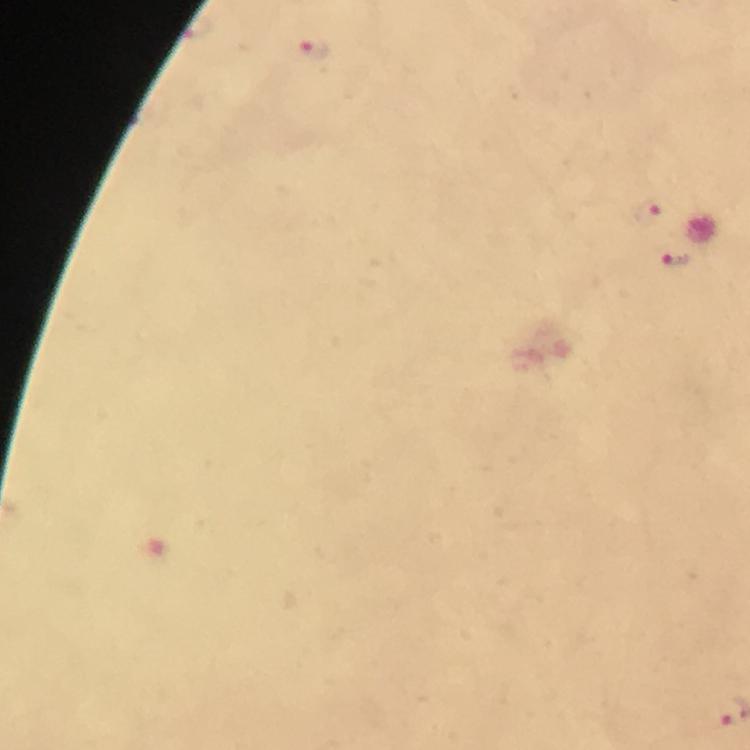
preparation = thick smear
capture = smartphone photograph through a microscope
malaria parasite locations = approximate centers as {x, y} in pixels: {316, 51}, {650, 211}, {675, 259}
context = from a diagnostic examination for malaria
magnification = 100x
cropped from = one field of view
image size = 750×750 pixels
immersion oil = applied
stain = Giemsa